State which parasite is depicted.
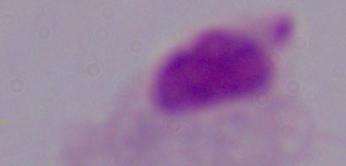

A trichomonad.

Summary:
  - Modality: micrograph
  - Magnification: 1000x